Assess this cell for malaria.
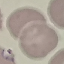
Parasitized.

Summary:
  - Image type: automatically extracted cell patch, resized to 64 × 64 pixels
  - Capture: smartphone camera at the microscope eyepiece
  - Stain: Giemsa
  - Preparation: thin blood smear